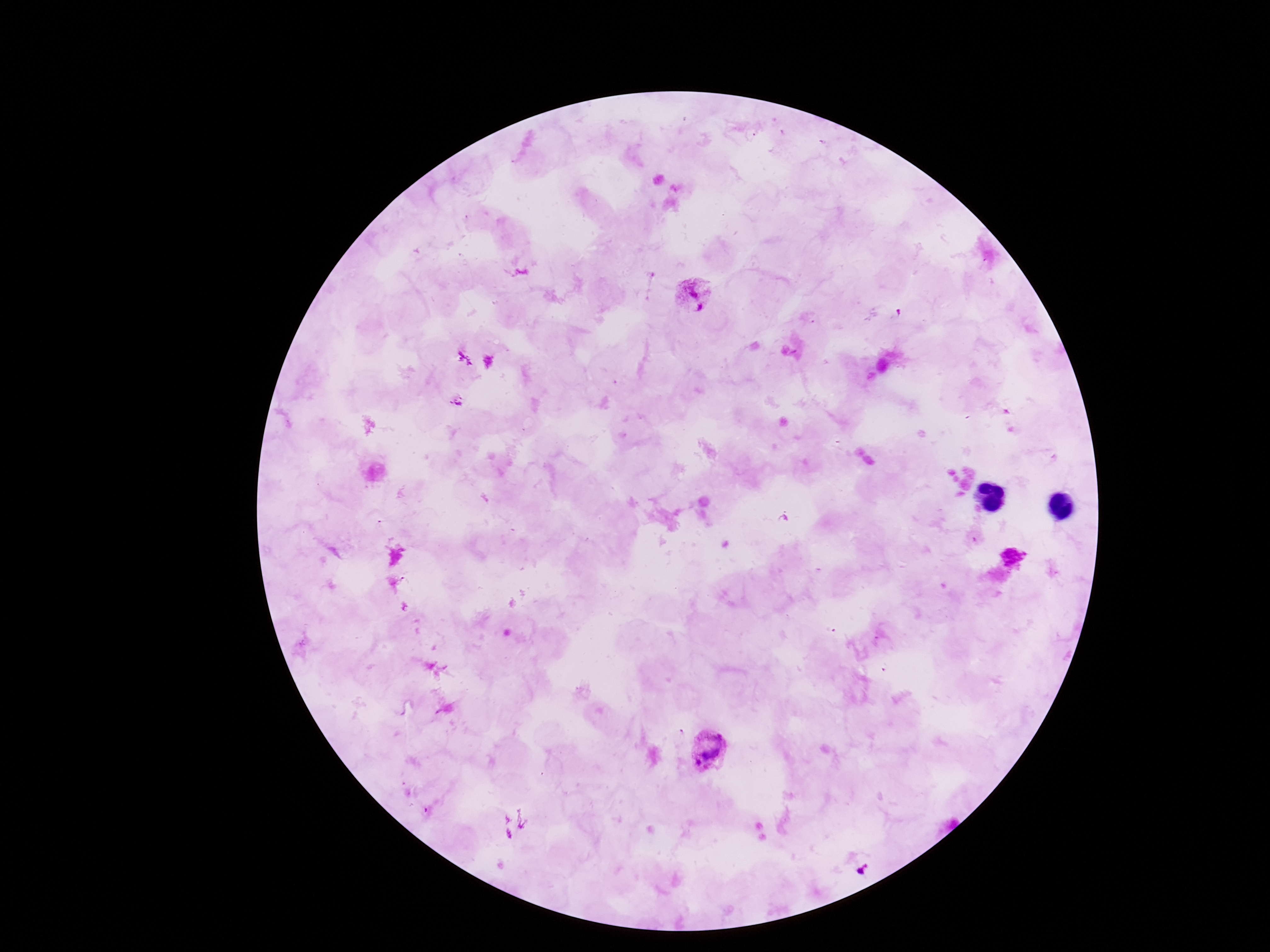
Approximate object centers, in pixels from the top-left corner. Plasmodium parasite locations: (x=694, y=295), (x=457, y=400), (x=1014, y=555), (x=712, y=752). Single field of view. Giemsa-stained preparation. Thick blood smear. Image is 1270×952 pixels. Photographed through the microscope eyepiece with a smartphone camera. Patient malaria status: infected. 100x magnification.